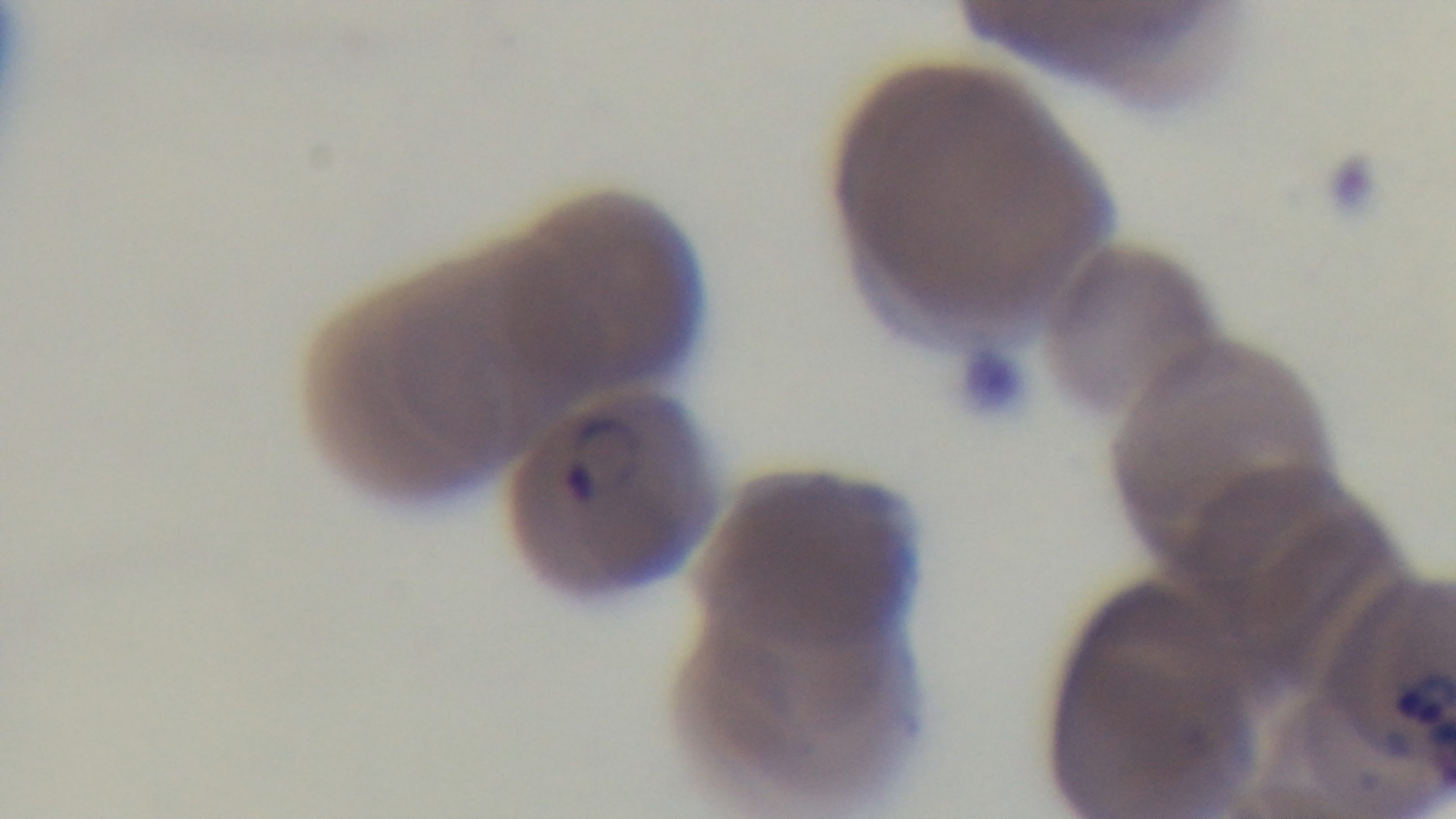
Summary:
  - Stain: Giemsa
  - Preparation: thin smear
  - Field of view: single
  - Objective: 100x oil immersion
  - Modality: light microscopy
  - Capture: mounted 4K digital camera
  - Malaria status: positive